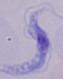
modality = micrograph
magnification = 1000x
identification = trypanosome